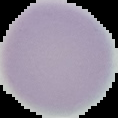
Summary:
  - Image type: cell region segmented out of the field of view; surrounding area masked to black
  - Image size: 118×118 pixels
  - Malaria status: uninfected
  - Preparation: thin blood smear